Outline each uninfected red blood cell.
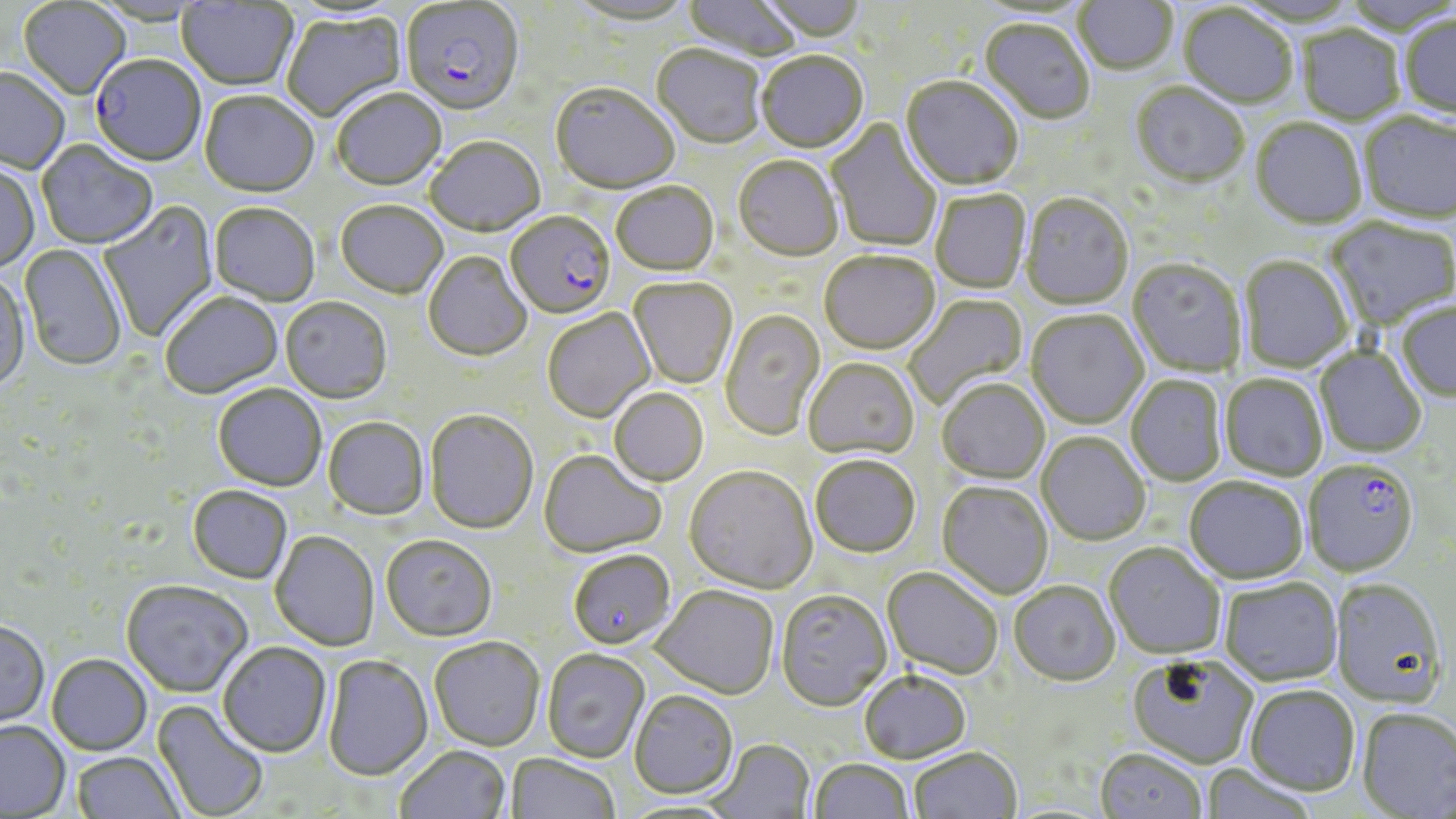
Approximate bounding boxes as named x1/y1/x2/y2 corners in pixels.
Uninfected red blood cells: (x1=567, y1=0, x2=698, y2=28), (x1=682, y1=0, x2=801, y2=63), (x1=757, y1=0, x2=868, y2=46), (x1=1074, y1=0, x2=1177, y2=77), (x1=18, y1=1, x2=131, y2=101), (x1=176, y1=1, x2=298, y2=92), (x1=973, y1=3, x2=1093, y2=23), (x1=1177, y1=5, x2=1297, y2=110), (x1=280, y1=12, x2=408, y2=124), (x1=1400, y1=15, x2=1456, y2=120), (x1=979, y1=20, x2=1095, y2=126), (x1=1296, y1=27, x2=1405, y2=127), (x1=652, y1=47, x2=766, y2=151), (x1=756, y1=53, x2=868, y2=155), (x1=0, y1=70, x2=69, y2=175), (x1=901, y1=78, x2=1023, y2=192), (x1=1131, y1=84, x2=1249, y2=190), (x1=550, y1=85, x2=679, y2=197), (x1=333, y1=90, x2=447, y2=192), (x1=199, y1=92, x2=319, y2=199), (x1=1358, y1=114, x2=1455, y2=226), (x1=826, y1=118, x2=942, y2=254), (x1=1250, y1=120, x2=1366, y2=232), (x1=424, y1=138, x2=545, y2=238), (x1=37, y1=141, x2=159, y2=250), (x1=733, y1=157, x2=843, y2=263), (x1=0, y1=163, x2=40, y2=274), (x1=611, y1=183, x2=719, y2=278), (x1=931, y1=189, x2=1031, y2=294), (x1=1020, y1=195, x2=1133, y2=311), (x1=98, y1=201, x2=218, y2=343), (x1=336, y1=201, x2=448, y2=299), (x1=209, y1=203, x2=320, y2=306), (x1=1325, y1=218, x2=1456, y2=331), (x1=19, y1=244, x2=128, y2=371), (x1=423, y1=251, x2=532, y2=361), (x1=818, y1=252, x2=941, y2=356), (x1=1239, y1=257, x2=1352, y2=374), (x1=1127, y1=260, x2=1247, y2=379), (x1=0, y1=271, x2=30, y2=392), (x1=629, y1=278, x2=738, y2=389), (x1=159, y1=291, x2=283, y2=398), (x1=903, y1=294, x2=1029, y2=410), (x1=280, y1=297, x2=392, y2=403), (x1=1396, y1=302, x2=1456, y2=403), (x1=542, y1=309, x2=655, y2=423), (x1=720, y1=310, x2=826, y2=442), (x1=1026, y1=311, x2=1148, y2=429), (x1=1314, y1=347, x2=1426, y2=458), (x1=803, y1=358, x2=919, y2=462), (x1=1220, y1=375, x2=1328, y2=481), (x1=1126, y1=376, x2=1227, y2=487), (x1=937, y1=380, x2=1050, y2=485), (x1=213, y1=384, x2=326, y2=491), (x1=609, y1=388, x2=709, y2=487), (x1=424, y1=409, x2=538, y2=534), (x1=323, y1=417, x2=428, y2=520), (x1=1036, y1=433, x2=1151, y2=546), (x1=538, y1=450, x2=667, y2=558), (x1=810, y1=456, x2=921, y2=559), (x1=684, y1=467, x2=818, y2=595), (x1=1184, y1=477, x2=1308, y2=584), (x1=937, y1=482, x2=1054, y2=600), (x1=188, y1=485, x2=293, y2=583), (x1=270, y1=531, x2=379, y2=650), (x1=381, y1=534, x2=498, y2=641), (x1=1104, y1=544, x2=1225, y2=661), (x1=568, y1=550, x2=675, y2=650), (x1=882, y1=568, x2=1003, y2=681), (x1=121, y1=579, x2=253, y2=697), (x1=1219, y1=579, x2=1343, y2=687), (x1=1331, y1=580, x2=1448, y2=710), (x1=1009, y1=582, x2=1120, y2=687), (x1=651, y1=585, x2=779, y2=700), (x1=776, y1=591, x2=892, y2=713), (x1=0, y1=620, x2=50, y2=727), (x1=429, y1=636, x2=545, y2=751), (x1=217, y1=641, x2=332, y2=757), (x1=542, y1=649, x2=650, y2=763), (x1=47, y1=653, x2=152, y2=755), (x1=322, y1=654, x2=433, y2=780), (x1=1127, y1=655, x2=1258, y2=769), (x1=859, y1=671, x2=971, y2=764), (x1=1245, y1=686, x2=1360, y2=798), (x1=629, y1=690, x2=738, y2=800), (x1=152, y1=700, x2=269, y2=819), (x1=1357, y1=708, x2=1456, y2=817), (x1=0, y1=720, x2=70, y2=817), (x1=707, y1=739, x2=814, y2=819), (x1=395, y1=745, x2=511, y2=819), (x1=909, y1=747, x2=1022, y2=819), (x1=1096, y1=749, x2=1206, y2=819), (x1=71, y1=751, x2=186, y2=818), (x1=505, y1=753, x2=621, y2=819), (x1=809, y1=759, x2=914, y2=819), (x1=1201, y1=765, x2=1317, y2=819).

{
  "plasmodium_falciparum_infected_red_blood_cell_locations": "approximate bounding boxes as named x1/y1/x2/y2 corners in pixels: (x1=399, y1=2, x2=525, y2=118), (x1=90, y1=56, x2=206, y2=168), (x1=504, y1=211, x2=615, y2=321), (x1=1304, y1=461, x2=1418, y2=578)",
  "slide_level_diagnosis": "Plasmodium falciparum",
  "image_size": "1456×819 pixels",
  "stain": "May-Grünwald-Giemsa",
  "magnification": "1000x",
  "preparation": "thin blood film",
  "modality": "light microscopy",
  "field_of_view": "single"
}